Report the malaria status of this cell.
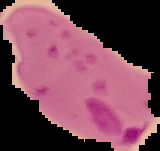
Parasitized.

Summary:
  - Image size: 160×151 pixels
  - Preparation: thin blood film
  - Image type: segmented cell region with the area outside set to black